Point out each Plasmodium parasite.
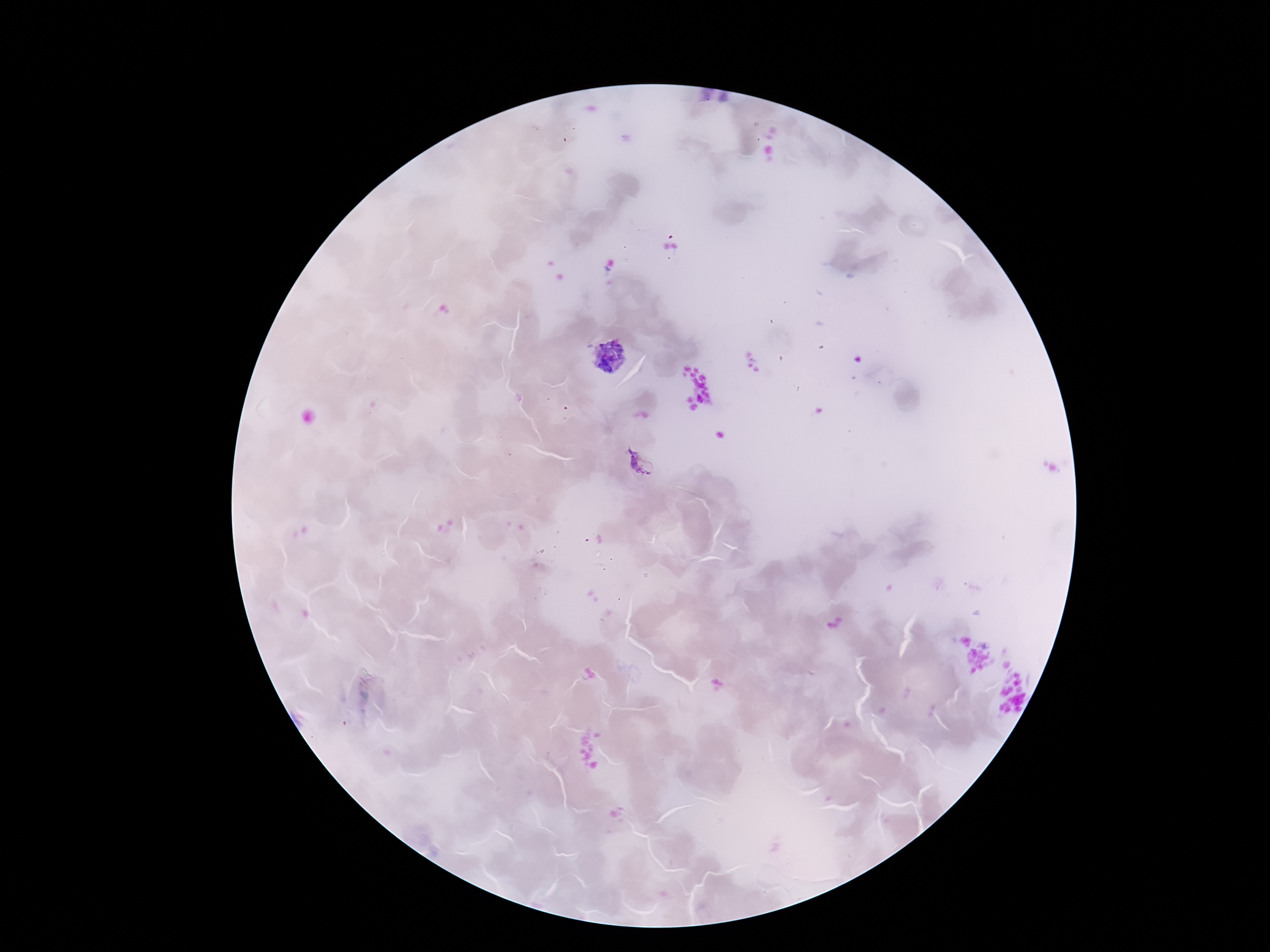

Approximate object centers, in pixels from the top-left corner.
Plasmodium parasites: (x=608, y=355), (x=641, y=465).

Summary:
  - Stain: Giemsa
  - Preparation: thick blood film
  - Image size: 1270×952 pixels
  - Magnification: 100x
  - Patient malaria status: positive
  - Capture: smartphone camera through the microscope eyepiece
  - Field of view: one from this slide